Comment on the morphology of the erythrocytes.
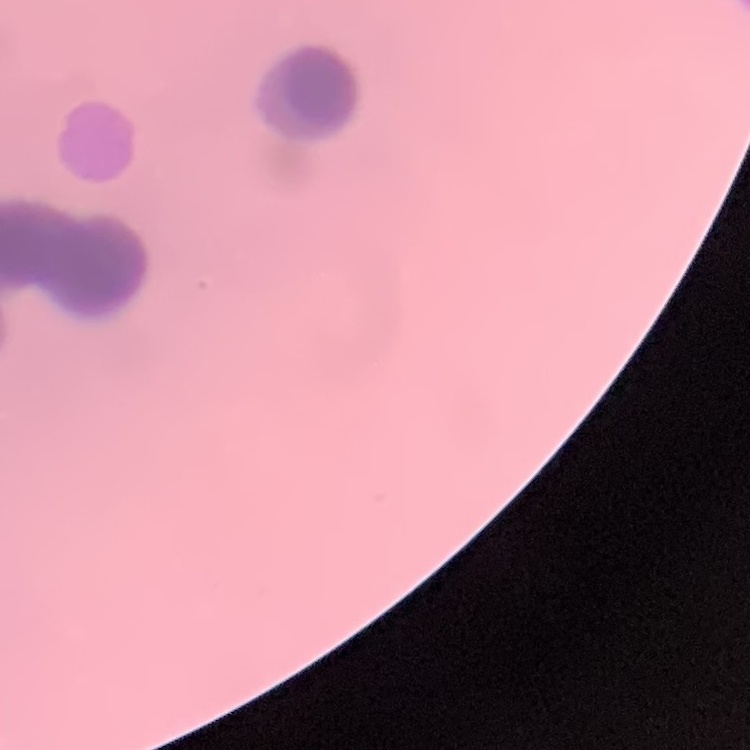

Rouleaux formation.

preparation = thin peripheral smear
stain = Field's or Giemsa
image type = square crop of a larger photomicrograph